Locate every Plasmodium parasite.
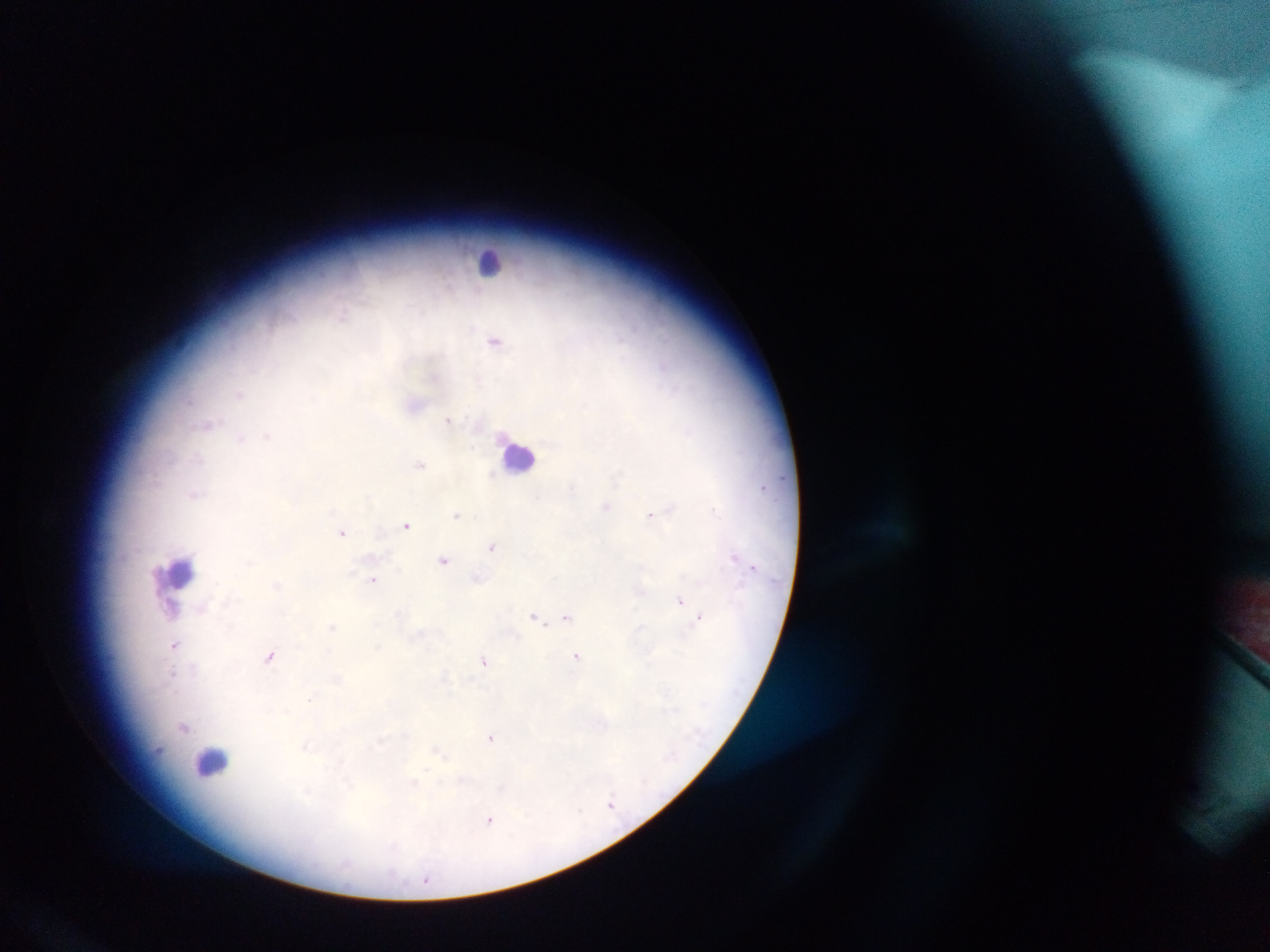
Approximate centers as [x, y] in pixels.
Plasmodium parasites: [342, 316], [495, 341], [664, 366], [239, 393], [189, 401], [448, 419], [209, 425], [689, 431], [268, 436], [240, 438], [420, 463], [491, 474], [762, 487], [572, 489], [606, 506], [671, 508], [713, 509], [457, 514], [650, 515], [406, 525], [343, 533], [491, 546], [735, 557], [444, 560], [754, 567], [477, 578], [373, 580], [277, 586], [680, 601], [172, 607], [202, 609], [534, 616], [567, 616], [699, 617], [332, 627], [175, 645], [378, 647], [269, 656], [576, 657], [485, 662], [172, 673], [444, 676], [310, 699], [183, 726], [490, 737], [380, 742], [437, 750], [157, 751], [414, 783], [611, 804], [580, 810], [490, 821], [426, 878].

country = Ghana
preparation = thick blood film
image size = 1270×952 pixels
leukocyte locations = approximate centers as [x, y] in pixels: [492, 262], [520, 455], [180, 572], [212, 761]
capture = mobile-phone photograph through a microscope
field of view = single